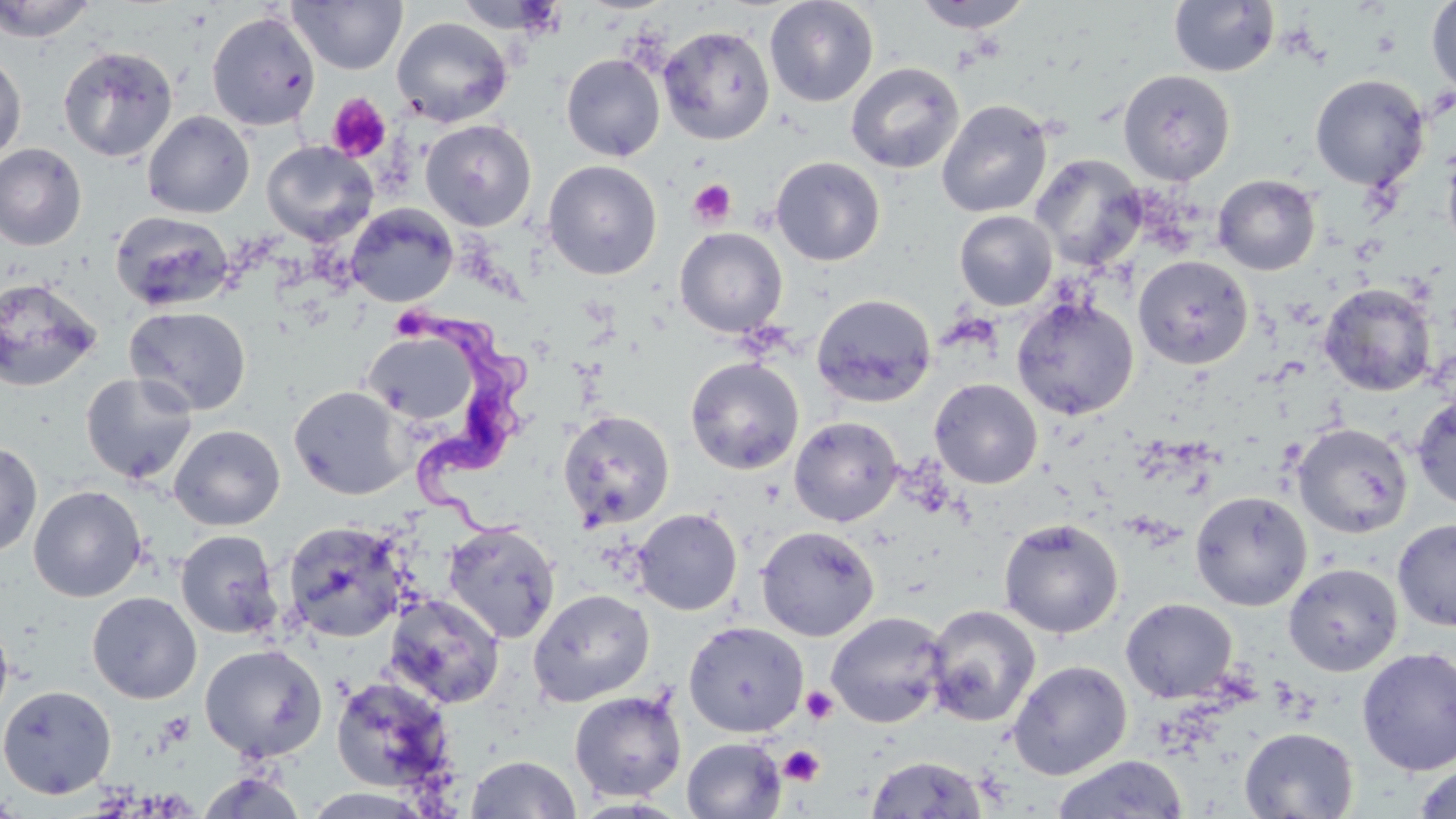
Approximate bounding boxes as named x1/y1/x2/y2 corners in pixels. Trypanosoma brucei locations: (x1=416, y1=302, x2=531, y2=545). Uninfected red blood cell locations: (x1=0, y1=0, x2=96, y2=43), (x1=288, y1=0, x2=407, y2=74), (x1=454, y1=0, x2=565, y2=34), (x1=764, y1=0, x2=879, y2=107), (x1=913, y1=0, x2=1033, y2=32), (x1=1168, y1=0, x2=1280, y2=77), (x1=1426, y1=0, x2=1456, y2=97), (x1=207, y1=10, x2=321, y2=131), (x1=392, y1=17, x2=513, y2=127), (x1=658, y1=25, x2=775, y2=145), (x1=58, y1=45, x2=178, y2=163), (x1=0, y1=53, x2=27, y2=162), (x1=561, y1=53, x2=666, y2=161), (x1=845, y1=61, x2=964, y2=174), (x1=1117, y1=69, x2=1237, y2=186), (x1=1309, y1=74, x2=1430, y2=191), (x1=936, y1=99, x2=1053, y2=218), (x1=142, y1=110, x2=255, y2=218), (x1=420, y1=119, x2=537, y2=232), (x1=1442, y1=136, x2=1456, y2=258), (x1=261, y1=140, x2=378, y2=245), (x1=0, y1=143, x2=87, y2=251), (x1=1029, y1=154, x2=1148, y2=271), (x1=770, y1=156, x2=885, y2=266), (x1=542, y1=160, x2=663, y2=280), (x1=1213, y1=174, x2=1321, y2=275), (x1=345, y1=203, x2=458, y2=308), (x1=954, y1=210, x2=1058, y2=311), (x1=110, y1=211, x2=235, y2=312), (x1=675, y1=227, x2=788, y2=337), (x1=1133, y1=256, x2=1254, y2=369), (x1=0, y1=277, x2=102, y2=392), (x1=1319, y1=283, x2=1437, y2=397), (x1=812, y1=293, x2=936, y2=408), (x1=1011, y1=297, x2=1139, y2=420), (x1=124, y1=306, x2=252, y2=416), (x1=364, y1=330, x2=480, y2=426), (x1=685, y1=356, x2=804, y2=475), (x1=80, y1=372, x2=198, y2=484), (x1=929, y1=378, x2=1043, y2=489), (x1=289, y1=385, x2=411, y2=500), (x1=1411, y1=395, x2=1456, y2=511), (x1=558, y1=410, x2=675, y2=531), (x1=789, y1=416, x2=903, y2=527), (x1=1292, y1=423, x2=1414, y2=539), (x1=169, y1=424, x2=285, y2=530), (x1=0, y1=440, x2=42, y2=558), (x1=29, y1=485, x2=147, y2=602), (x1=1189, y1=491, x2=1312, y2=611), (x1=633, y1=508, x2=742, y2=615), (x1=999, y1=518, x2=1123, y2=638), (x1=1393, y1=518, x2=1456, y2=631), (x1=282, y1=521, x2=410, y2=643), (x1=443, y1=521, x2=560, y2=644), (x1=756, y1=525, x2=879, y2=641), (x1=176, y1=530, x2=282, y2=639), (x1=1283, y1=562, x2=1402, y2=676), (x1=528, y1=589, x2=654, y2=707), (x1=87, y1=591, x2=202, y2=704), (x1=384, y1=593, x2=505, y2=709), (x1=1121, y1=597, x2=1238, y2=703), (x1=924, y1=605, x2=1041, y2=727), (x1=825, y1=611, x2=949, y2=728), (x1=0, y1=616, x2=13, y2=726), (x1=684, y1=621, x2=808, y2=737), (x1=200, y1=644, x2=327, y2=762), (x1=1357, y1=647, x2=1456, y2=776), (x1=1007, y1=660, x2=1132, y2=779), (x1=330, y1=676, x2=457, y2=794), (x1=0, y1=684, x2=117, y2=800), (x1=569, y1=690, x2=688, y2=802), (x1=1239, y1=727, x2=1359, y2=818), (x1=681, y1=737, x2=786, y2=819), (x1=465, y1=754, x2=581, y2=818), (x1=1052, y1=754, x2=1190, y2=819), (x1=866, y1=755, x2=988, y2=818), (x1=1414, y1=763, x2=1456, y2=819), (x1=197, y1=770, x2=308, y2=818), (x1=300, y1=788, x2=434, y2=818). Platelet locations: (x1=327, y1=93, x2=392, y2=161), (x1=688, y1=179, x2=737, y2=227), (x1=397, y1=305, x2=428, y2=343), (x1=801, y1=686, x2=838, y2=724), (x1=778, y1=745, x2=825, y2=787). Slide-level diagnosis: Trypanosoma brucei. Thin blood film. Image is 1456×819 pixels. May-Grünwald-Giemsa stain. Light microscopy. 1000x magnification. Single field of view.